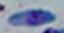
1000x magnification. Photomicrograph. Toxoplasma gondii is shown.